Assess this cell for malaria.
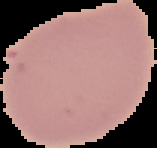
It is uninfected.

Summary:
  - Image type: segmented cell region on a black background
  - Image size: 157×148 pixels
  - Preparation: thin blood film